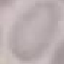

Summary:
  - Result: no malaria parasites seen
  - Capture: smartphone through the microscope eyepiece
  - Image type: automatically extracted cell patch, resized to 64 × 64 pixels
  - Preparation: thin blood smear
  - Stain: Giemsa